Classify this cell by malaria status.
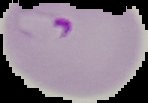
It is parasitized.

Cell region segmented out of the field of view; the surrounding area is masked to black. Image is 148×103 pixels. From a thin blood smear.